State which parasite is depicted.
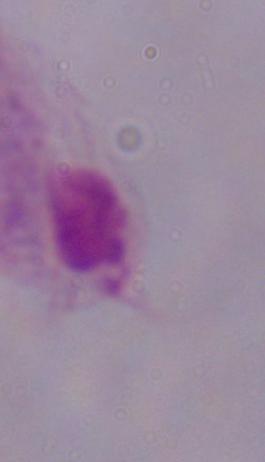

A trichomonad.

Captured at 1000x magnification. Micrograph.